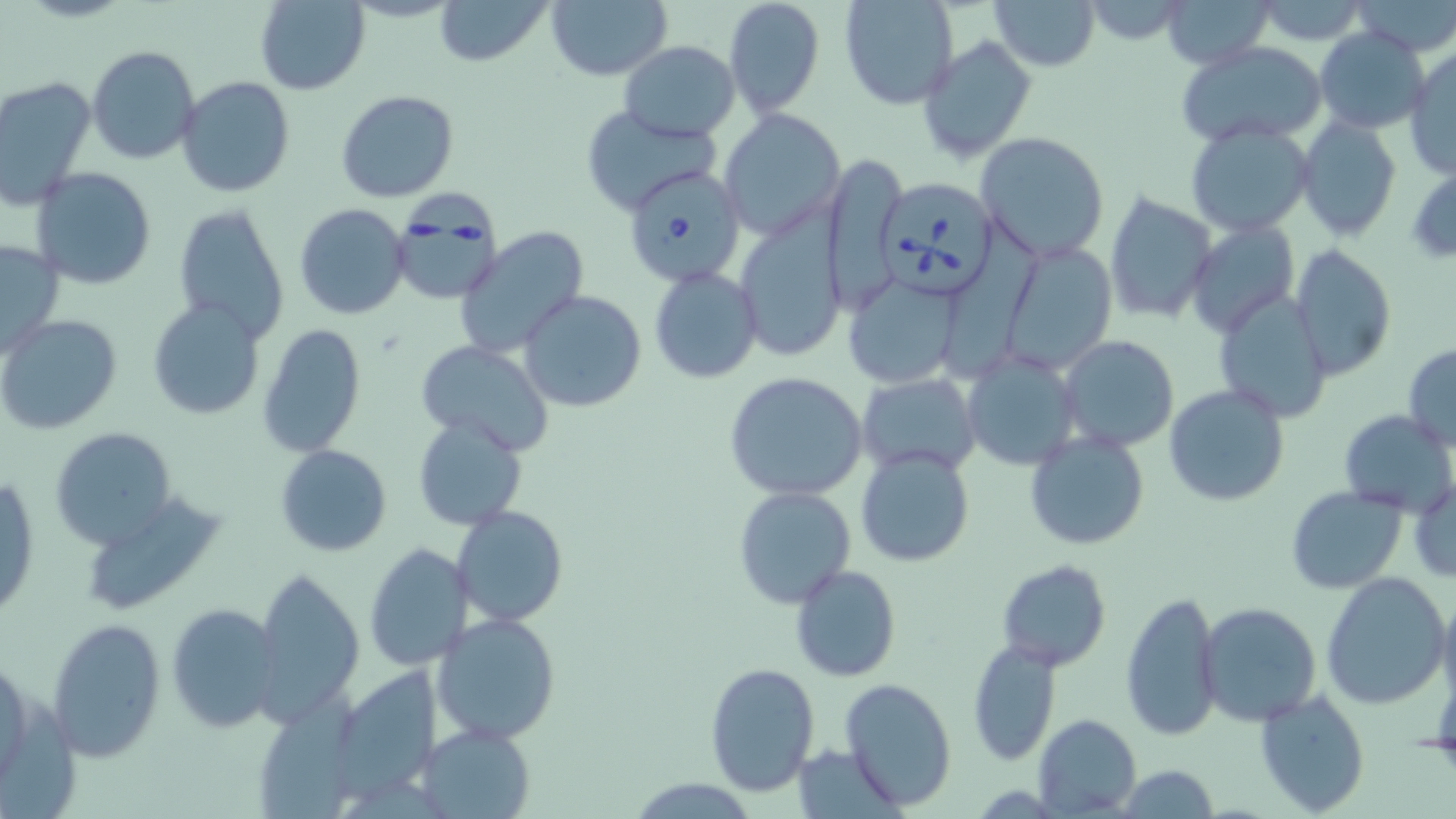
Approximate bounding boxes as (x1,y1)-(x2,y2) corner pairs in pixels. Uninfected red blood cell locations: (431,0)-(554,67), (545,0)-(673,82), (724,0)-(825,117), (839,0)-(959,110), (991,0)-(1102,71), (1161,0)-(1277,69), (1351,0)-(1456,55), (253,1)-(370,94), (1082,1)-(1197,47), (1252,2)-(1374,46), (1314,28)-(1430,134), (916,35)-(1038,163), (619,40)-(740,141), (1178,40)-(1330,150), (87,45)-(200,165), (1405,46)-(1456,180), (1,76)-(97,209), (176,76)-(296,199), (335,91)-(458,204), (579,105)-(722,216), (718,108)-(844,241), (1297,115)-(1401,240), (1185,121)-(1313,236), (975,130)-(1110,263), (822,151)-(908,304), (31,166)-(156,289), (1103,190)-(1217,325), (172,203)-(289,341), (293,203)-(411,320), (731,208)-(847,362), (942,212)-(1043,376), (1188,220)-(1298,340), (452,226)-(591,360), (0,237)-(66,359), (999,240)-(1119,374), (1288,245)-(1397,380), (649,266)-(763,383), (841,270)-(967,390), (519,290)-(647,413), (1211,293)-(1332,423), (145,299)-(266,421), (1,314)-(123,436), (258,324)-(368,457), (1058,335)-(1180,454), (416,338)-(553,454), (1403,342)-(1456,449), (961,347)-(1084,472), (988,367)-(1110,508), (724,373)-(870,502), (859,373)-(982,474), (1162,383)-(1290,505), (1338,409)-(1456,517), (410,416)-(528,531), (49,428)-(179,549), (1024,431)-(1149,550), (275,445)-(392,556), (856,447)-(974,568), (1,476)-(40,621), (1410,476)-(1456,584), (733,486)-(857,610), (1285,486)-(1407,594), (79,492)-(228,617), (453,506)-(567,628), (363,544)-(473,673), (996,559)-(1111,671), (791,565)-(900,681), (253,568)-(364,721), (1321,572)-(1450,708), (1437,590)-(1456,713), (1121,591)-(1222,741), (166,601)-(282,733), (1197,601)-(1321,725), (432,612)-(562,745), (46,615)-(168,761), (968,640)-(1061,766), (702,661)-(820,797), (342,668)-(442,800), (840,677)-(956,809), (264,685)-(369,819), (1253,689)-(1372,816), (1033,713)-(1141,817), (418,724)-(535,818), (796,744)-(901,817), (1114,765)-(1221,819). Babesia divergens-infected red blood cell locations: (621,161)-(748,290), (881,175)-(997,297), (391,189)-(499,304). Slide-level diagnosis: Babesia divergens. Light microscopy. One field of a larger specimen. Thin blood film. May-Grünwald-Giemsa-stained preparation. 1000x magnification. Image is 1456×819 pixels.